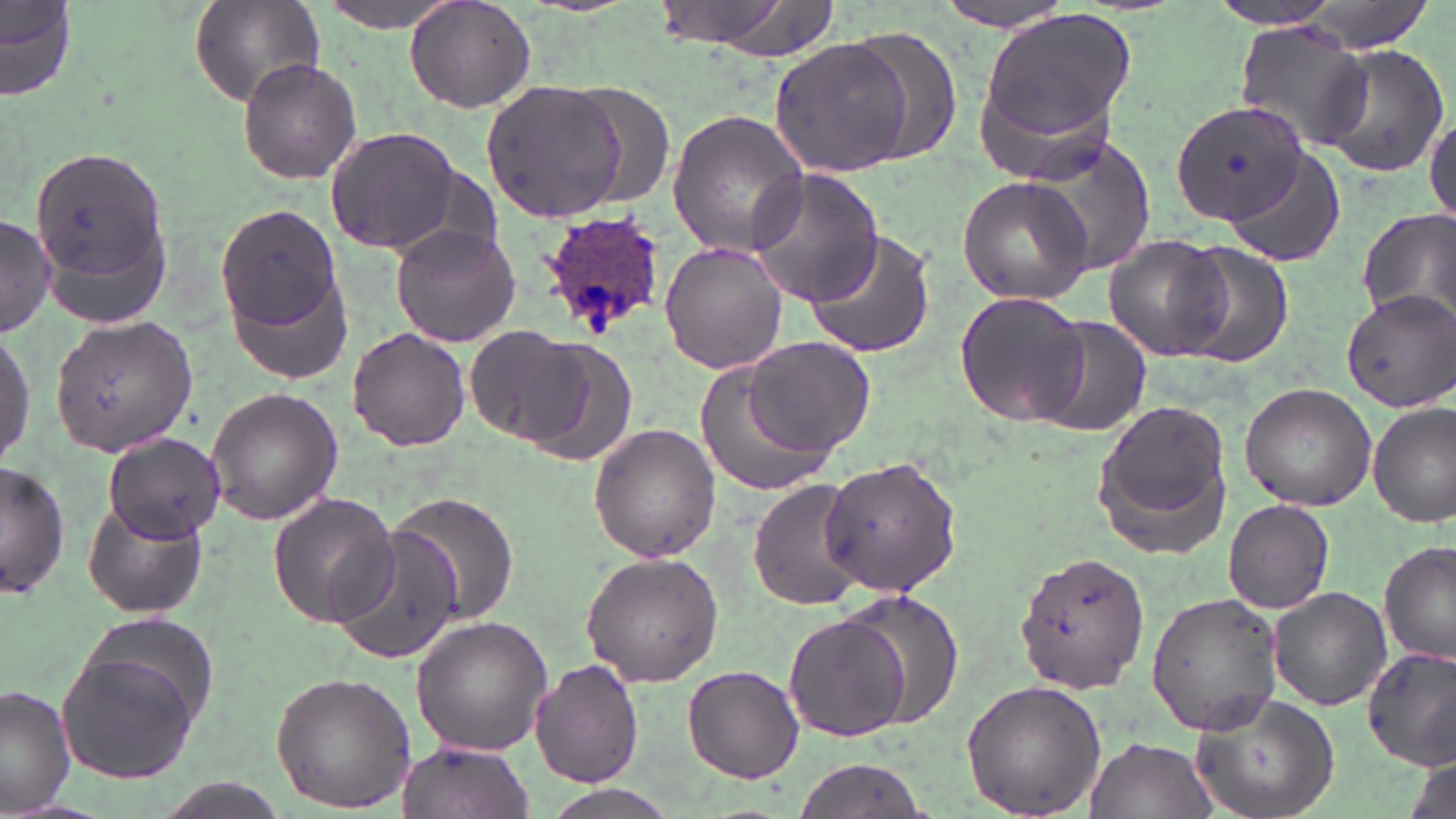

{
  "slide_level_diagnosis": "Plasmodium ovale",
  "magnification": "1000x",
  "plasmodium_ovale_infected_red_blood_cell_locations": "approximate bounding boxes as (x1, y1, x2, y2) in pixels: (541, 212, 666, 334)",
  "modality": "optical microscopy",
  "preparation": "thin blood film",
  "uninfected_red_blood_cell_locations": "approximate bounding boxes as (x1, y1, x2, y2) in pixels: (0, 0, 75, 104), (190, 0, 324, 110), (661, 0, 837, 63), (934, 0, 1076, 32), (1208, 0, 1353, 31), (405, 1, 536, 113), (313, 2, 462, 33), (977, 9, 1137, 150), (1232, 22, 1375, 151), (840, 27, 965, 166), (771, 36, 918, 177), (1312, 45, 1450, 180), (235, 56, 362, 184), (483, 78, 630, 223), (1169, 99, 1306, 225), (667, 107, 811, 258), (1426, 109, 1456, 225), (323, 125, 463, 256), (1023, 131, 1161, 283), (27, 145, 174, 298), (1223, 147, 1347, 268), (746, 169, 884, 306), (957, 175, 1095, 305), (212, 201, 347, 359), (1356, 210, 1456, 333), (0, 216, 56, 336), (391, 224, 521, 348), (801, 230, 935, 361), (1103, 234, 1232, 363), (1169, 240, 1294, 367), (660, 241, 785, 374), (1341, 289, 1456, 409), (954, 291, 1094, 429), (50, 317, 199, 454), (1039, 318, 1151, 438), (0, 325, 35, 468), (347, 327, 470, 451), (466, 328, 593, 446), (744, 336, 876, 457), (698, 360, 838, 497), (1240, 383, 1376, 509), (206, 386, 343, 526), (1094, 397, 1235, 550), (1369, 399, 1454, 528), (589, 423, 721, 562), (102, 432, 229, 545), (819, 453, 962, 597), (1, 460, 68, 601), (751, 479, 869, 612), (388, 491, 520, 625), (267, 493, 401, 627), (1223, 498, 1334, 613), (82, 499, 207, 620), (329, 524, 462, 667), (1378, 541, 1455, 667), (1015, 551, 1152, 693), (579, 552, 724, 686), (1268, 586, 1390, 712), (837, 589, 966, 726), (1146, 591, 1285, 736), (784, 612, 911, 742), (77, 615, 222, 733), (410, 615, 554, 756), (56, 644, 205, 786), (1361, 646, 1456, 772), (531, 659, 644, 788), (682, 664, 803, 784), (269, 671, 417, 813), (961, 679, 1107, 817), (1, 686, 76, 815), (1190, 692, 1339, 819), (1084, 734, 1215, 819), (396, 738, 534, 819), (1406, 755, 1453, 819), (792, 759, 926, 819), (542, 785, 676, 819)",
  "image_size": "1456×819 pixels",
  "stain": "May-Grünwald-Giemsa",
  "field_of_view": "single"
}